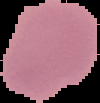
Cell region segmented out of the field of view; the surrounding area is masked to black. Image is 100×103 pixels. From a thin blood smear. Malaria status: uninfected.